Describe the morphology of the erythrocytes.
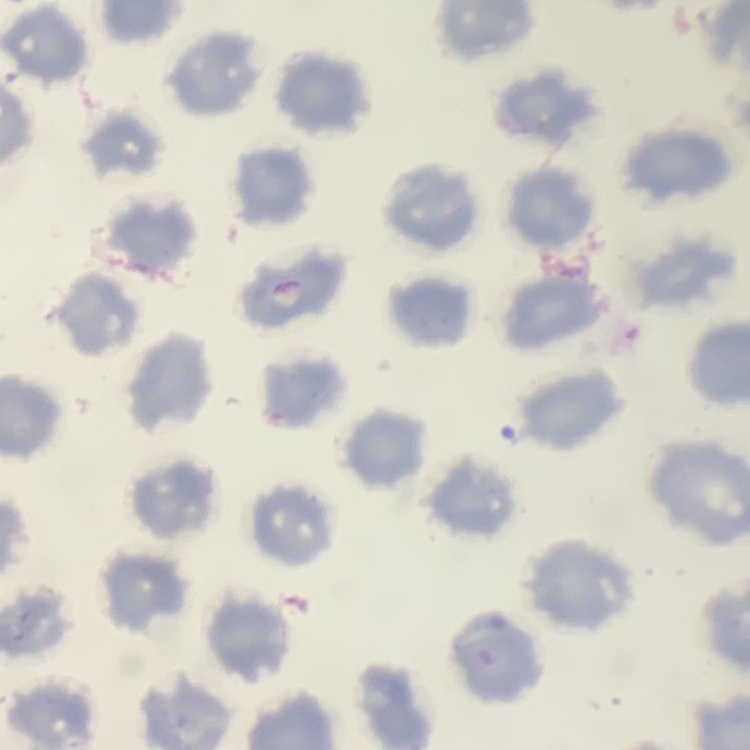
They show no rouleaux formation.

Summary:
  - Preparation: thin blood smear
  - Stain: Field's or Giemsa
  - Image type: one tile cut from a larger photomicrograph